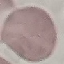

malaria_status: uninfected
preparation: thin blood smear
capture: smartphone through the microscope eyepiece
image_type: automatically extracted cell patch, resized to 64 × 64 pixels
stain: Giemsa